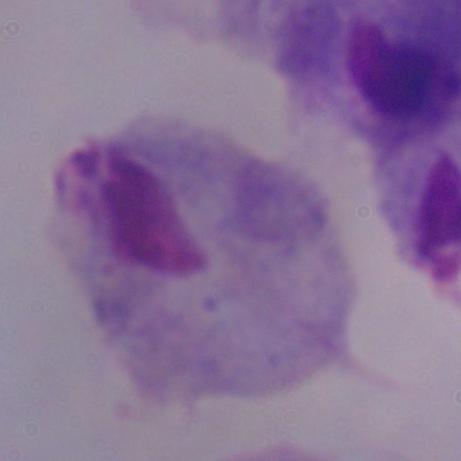

{
  "modality": "photomicrograph",
  "identification": "trichomonad",
  "magnification": "1000x"
}